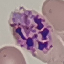 Result: malaria parasites detected. Thin smear of blood. Acquired by smartphone through the microscope eyepiece. Giemsa-stained preparation. Cell patch, automatically extracted from a larger field of view and resized to 64 × 64 pixels.